Assess this cell for malaria.
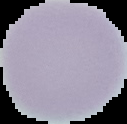

It is uninfected.

From a thin blood film. Image is 127×124 pixels. Cell region segmented out of the field of view; the surrounding area is masked to black.